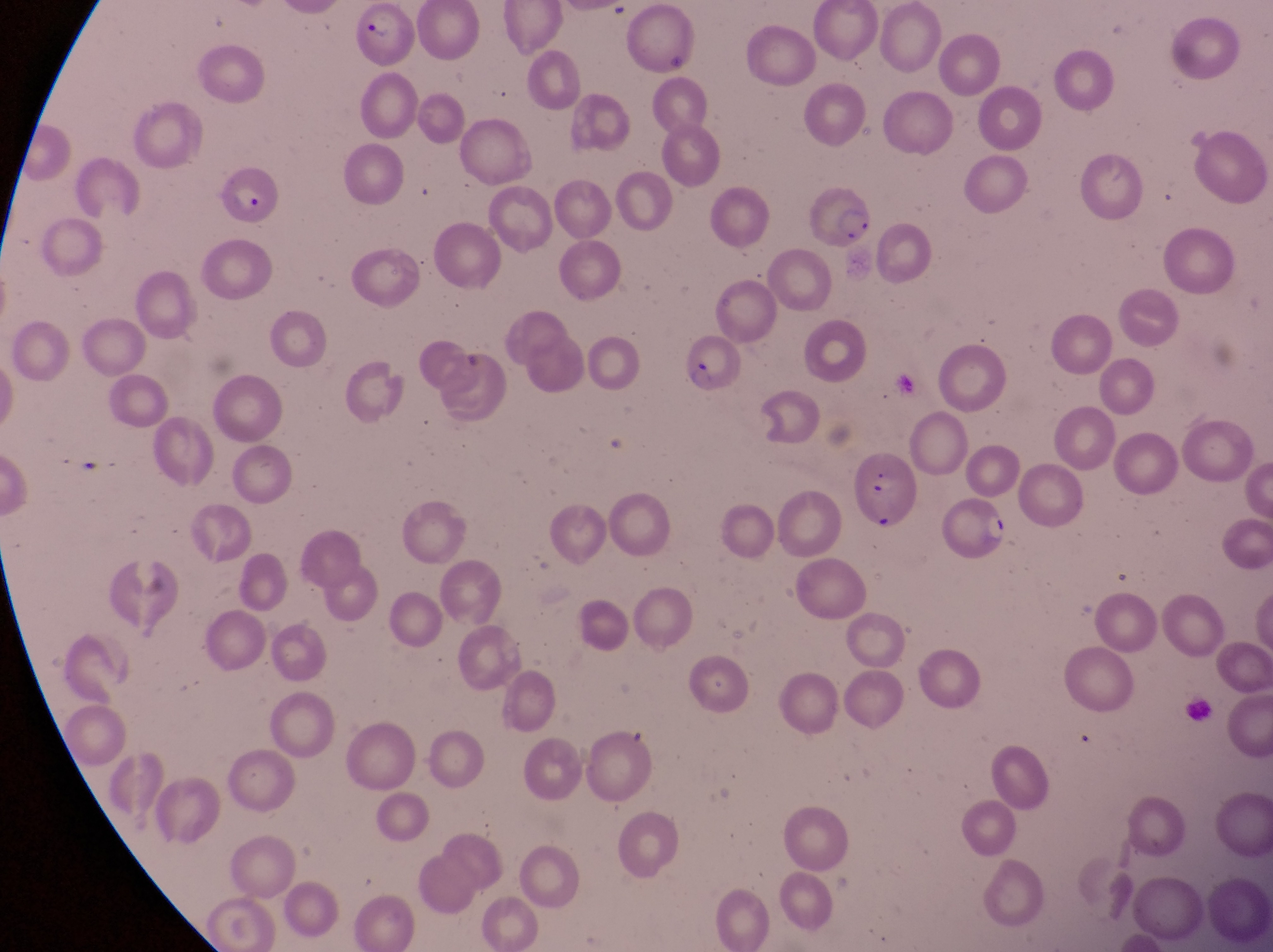

Approximate bounding boxes as [left, top, right, bottom] in pixels.
Summary:
  - Artifact (platelet-like body, stain precipitate, or debris) locations: [659, 47, 689, 77]
  - Parasitised red blood cell locations: [352, 2, 419, 69], [218, 167, 285, 232], [808, 177, 882, 255], [676, 329, 739, 396], [851, 460, 914, 535], [934, 495, 1011, 569]
  - Magnification: 1000x
  - Field of view: single
  - Image size: 1273×952 pixels
  - Preparation: thin blood smear
  - Capture: smartphone photograph through the eyepiece of an Olympus CX-23 microscope
  - Country: Uganda